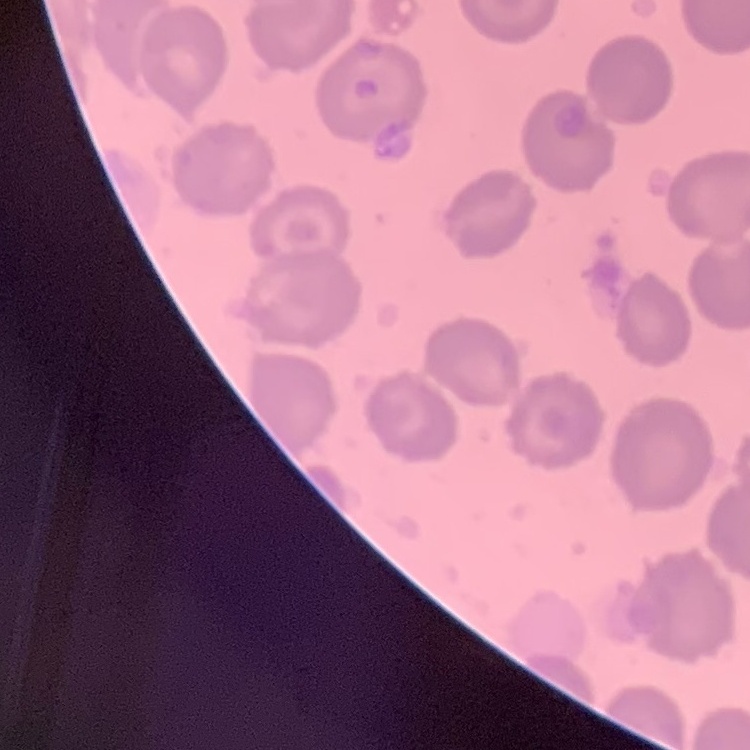

Summary:
  - Erythrocyte morphology: no rouleaux formation
  - Stain: Field's or Giemsa
  - Preparation: thin blood smear
  - Image type: square crop of a larger photomicrograph